State which parasite is depicted.
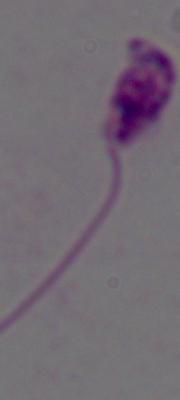
This is Leishmania.

Micrograph. Captured at 1000x magnification.